Report the malaria status of this cell.
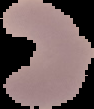

It is parasitized.

preparation = thin blood film
image size = 94×109 pixels
image type = segmented cell region on a black background